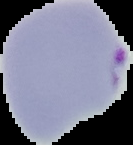
Summary:
  - Result: Plasmodium parasites detected
  - Image type: cell region segmented out of the field of view; surrounding area masked to black
  - Image size: 133×145 pixels
  - Preparation: thin blood smear